Give the preparation type.
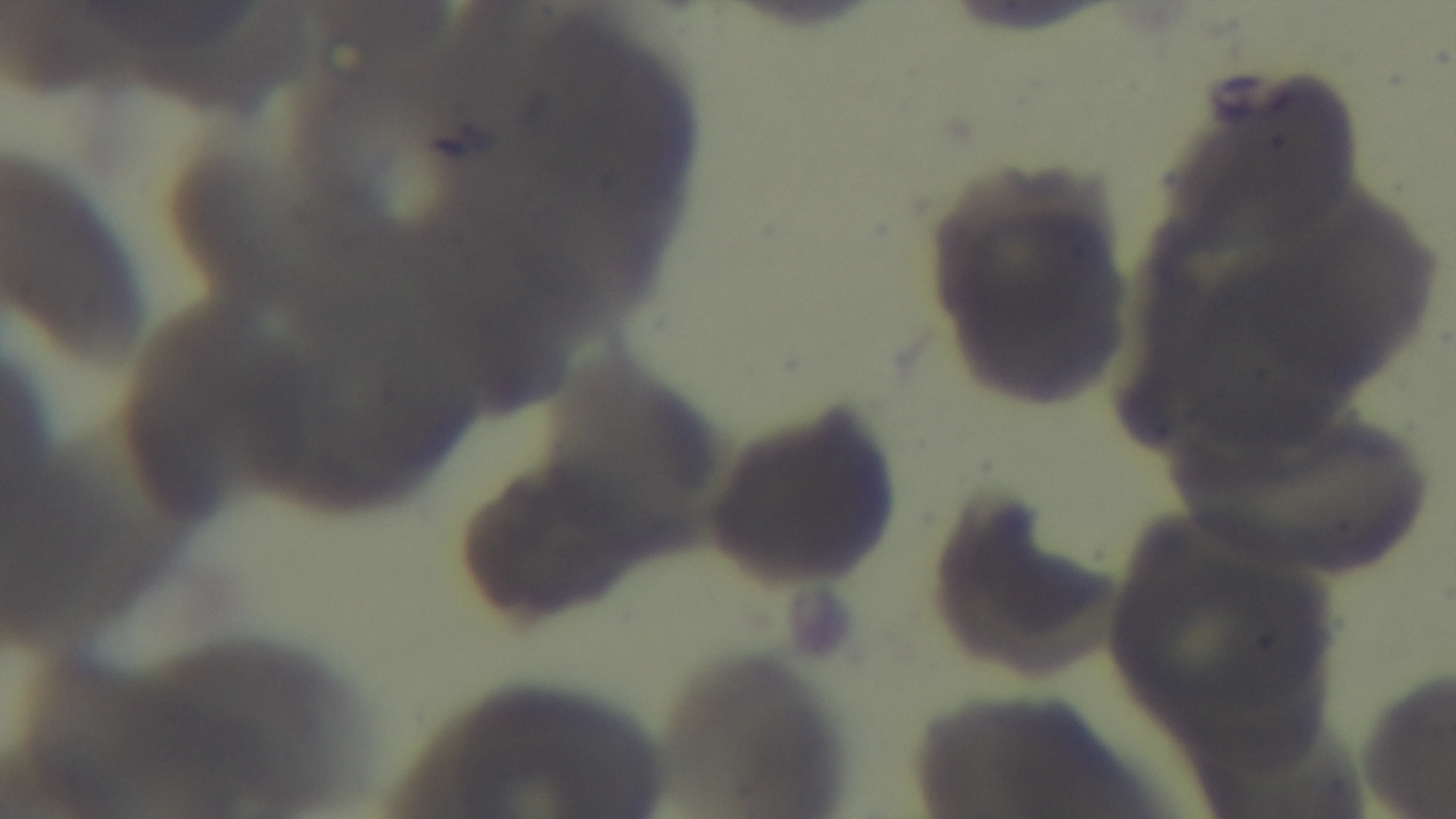
A thin smear.

Summary:
  - Objective: 100x oil immersion
  - Capture: mounted 4K digital camera
  - Modality: light microscopy
  - Field of view: single
  - Malaria status: negative
  - Stain: Giemsa